Assess the morphology of the erythrocytes.
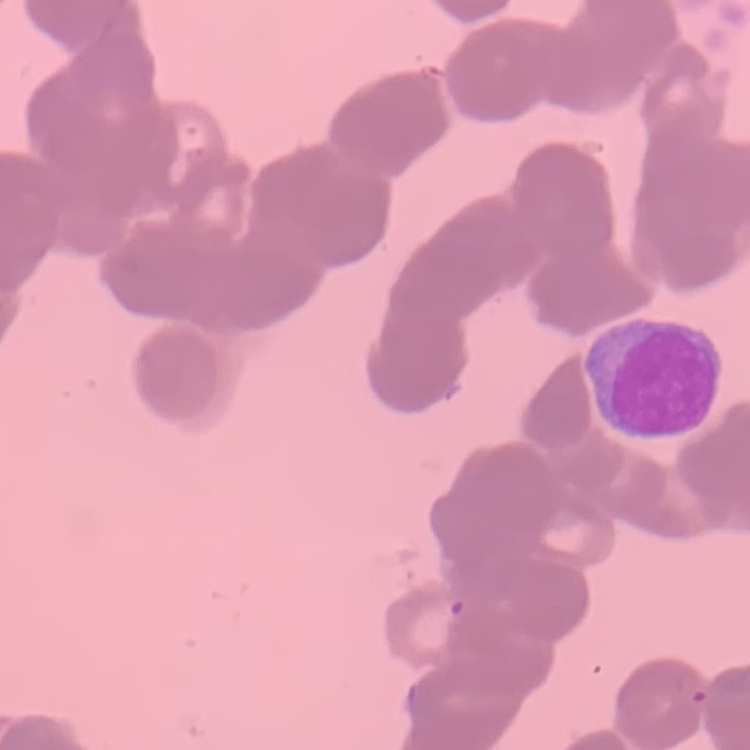
Rouleaux formation.

{
  "stain": "Field's or Giemsa",
  "preparation": "thin peripheral smear",
  "image_type": "one tile cut from a larger photomicrograph"
}